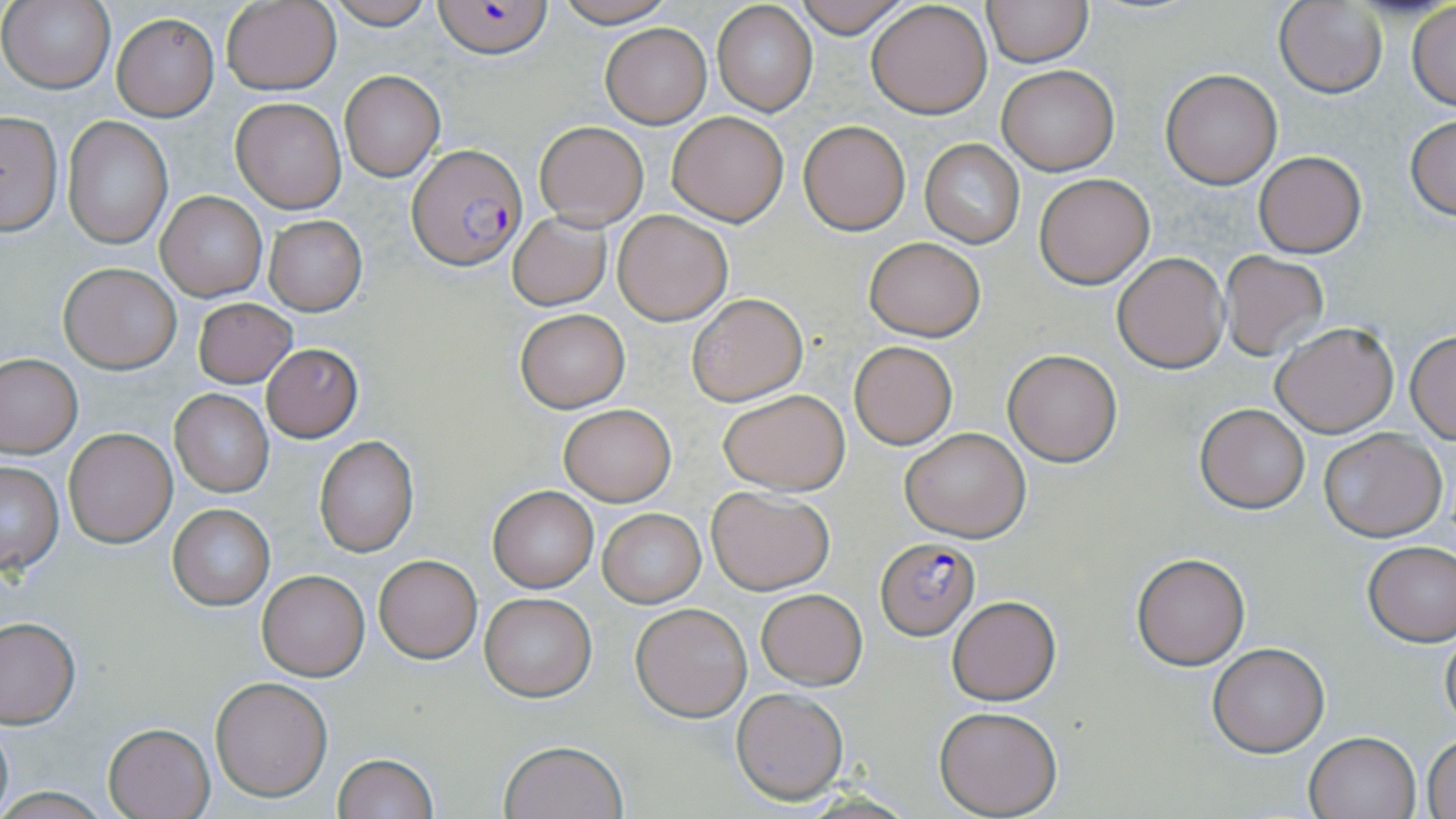

slide-level diagnosis = Plasmodium falciparum
magnification = 1000x
uninfected red blood cell locations = approximate bounding boxes as named x1/y1/x2/y2 corners in pixels: (x1=2, y1=0, x2=114, y2=93), (x1=326, y1=0, x2=436, y2=28), (x1=550, y1=0, x2=677, y2=27), (x1=792, y1=0, x2=913, y2=37), (x1=983, y1=0, x2=1091, y2=67), (x1=221, y1=1, x2=341, y2=95), (x1=867, y1=1, x2=992, y2=119), (x1=1274, y1=2, x2=1387, y2=98), (x1=712, y1=3, x2=817, y2=116), (x1=1407, y1=3, x2=1456, y2=110), (x1=112, y1=13, x2=218, y2=120), (x1=600, y1=23, x2=710, y2=128), (x1=998, y1=64, x2=1118, y2=175), (x1=339, y1=69, x2=446, y2=182), (x1=1160, y1=69, x2=1283, y2=188), (x1=231, y1=97, x2=346, y2=213), (x1=0, y1=111, x2=64, y2=235), (x1=667, y1=111, x2=788, y2=225), (x1=1405, y1=114, x2=1456, y2=220), (x1=62, y1=116, x2=172, y2=251), (x1=799, y1=120, x2=910, y2=235), (x1=534, y1=121, x2=648, y2=230), (x1=920, y1=139, x2=1023, y2=247), (x1=1253, y1=150, x2=1366, y2=257), (x1=1033, y1=174, x2=1154, y2=289), (x1=156, y1=192, x2=266, y2=301), (x1=614, y1=210, x2=732, y2=324), (x1=507, y1=211, x2=612, y2=310), (x1=263, y1=215, x2=367, y2=315), (x1=864, y1=237, x2=985, y2=341), (x1=1112, y1=251, x2=1229, y2=374), (x1=1220, y1=252, x2=1330, y2=362), (x1=57, y1=262, x2=182, y2=372), (x1=686, y1=292, x2=808, y2=407), (x1=192, y1=297, x2=298, y2=387), (x1=513, y1=308, x2=631, y2=412), (x1=1270, y1=320, x2=1400, y2=438), (x1=1406, y1=331, x2=1456, y2=442), (x1=850, y1=341, x2=956, y2=449), (x1=260, y1=344, x2=363, y2=441), (x1=1002, y1=349, x2=1123, y2=466), (x1=0, y1=355, x2=81, y2=456), (x1=718, y1=388, x2=849, y2=494), (x1=171, y1=389, x2=272, y2=496), (x1=559, y1=402, x2=677, y2=506), (x1=1194, y1=402, x2=1309, y2=513), (x1=900, y1=427, x2=1030, y2=541), (x1=64, y1=428, x2=176, y2=548), (x1=1319, y1=429, x2=1447, y2=542), (x1=314, y1=436, x2=419, y2=557), (x1=0, y1=460, x2=64, y2=575), (x1=706, y1=485, x2=834, y2=595), (x1=488, y1=486, x2=598, y2=592), (x1=167, y1=503, x2=275, y2=610), (x1=599, y1=509, x2=705, y2=606), (x1=1361, y1=541, x2=1456, y2=646), (x1=1132, y1=551, x2=1250, y2=669), (x1=374, y1=554, x2=483, y2=663), (x1=258, y1=571, x2=370, y2=681), (x1=755, y1=588, x2=867, y2=689), (x1=479, y1=592, x2=597, y2=701), (x1=948, y1=596, x2=1061, y2=705), (x1=631, y1=602, x2=752, y2=721), (x1=0, y1=617, x2=80, y2=728), (x1=1440, y1=622, x2=1456, y2=737), (x1=1207, y1=642, x2=1330, y2=757), (x1=211, y1=676, x2=332, y2=801), (x1=732, y1=689, x2=847, y2=802), (x1=935, y1=706, x2=1062, y2=817), (x1=0, y1=716, x2=14, y2=819), (x1=102, y1=722, x2=216, y2=818), (x1=1304, y1=730, x2=1420, y2=818), (x1=1423, y1=735, x2=1456, y2=819), (x1=500, y1=740, x2=627, y2=819), (x1=332, y1=753, x2=438, y2=819)
modality = light microscopy
preparation = thin blood film
field of view = single
stain = May-Grünwald-Giemsa
image size = 1456×819 pixels
Plasmodium falciparum-infected red blood cell locations = approximate bounding boxes as named x1/y1/x2/y2 corners in pixels: (x1=432, y1=1, x2=554, y2=58), (x1=408, y1=145, x2=526, y2=271), (x1=875, y1=538, x2=978, y2=637)